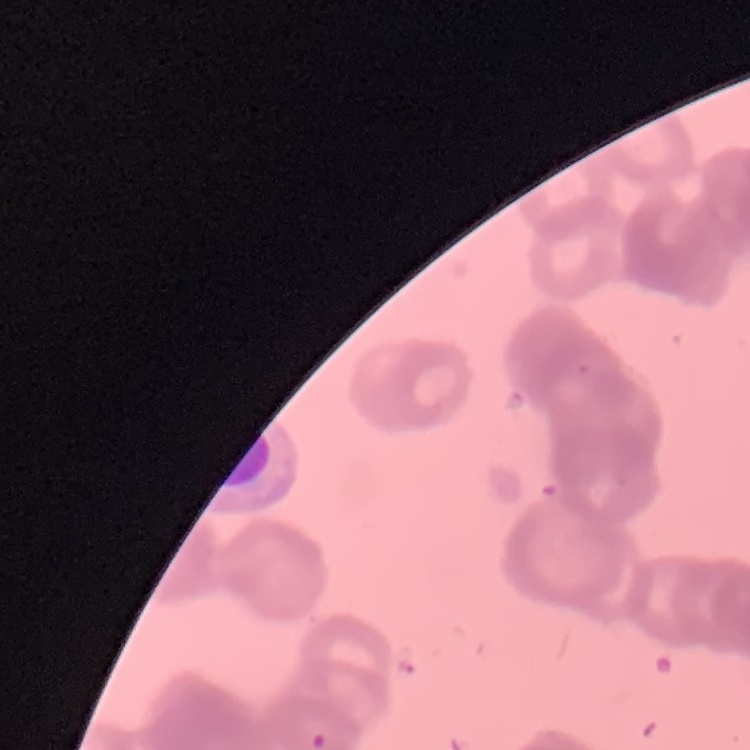 The red blood cells show rouleaux formation. Field's or Giemsa stain. Thin blood smear. Square crop of a larger photomicrograph.